Outline each blood parasite and name the species.
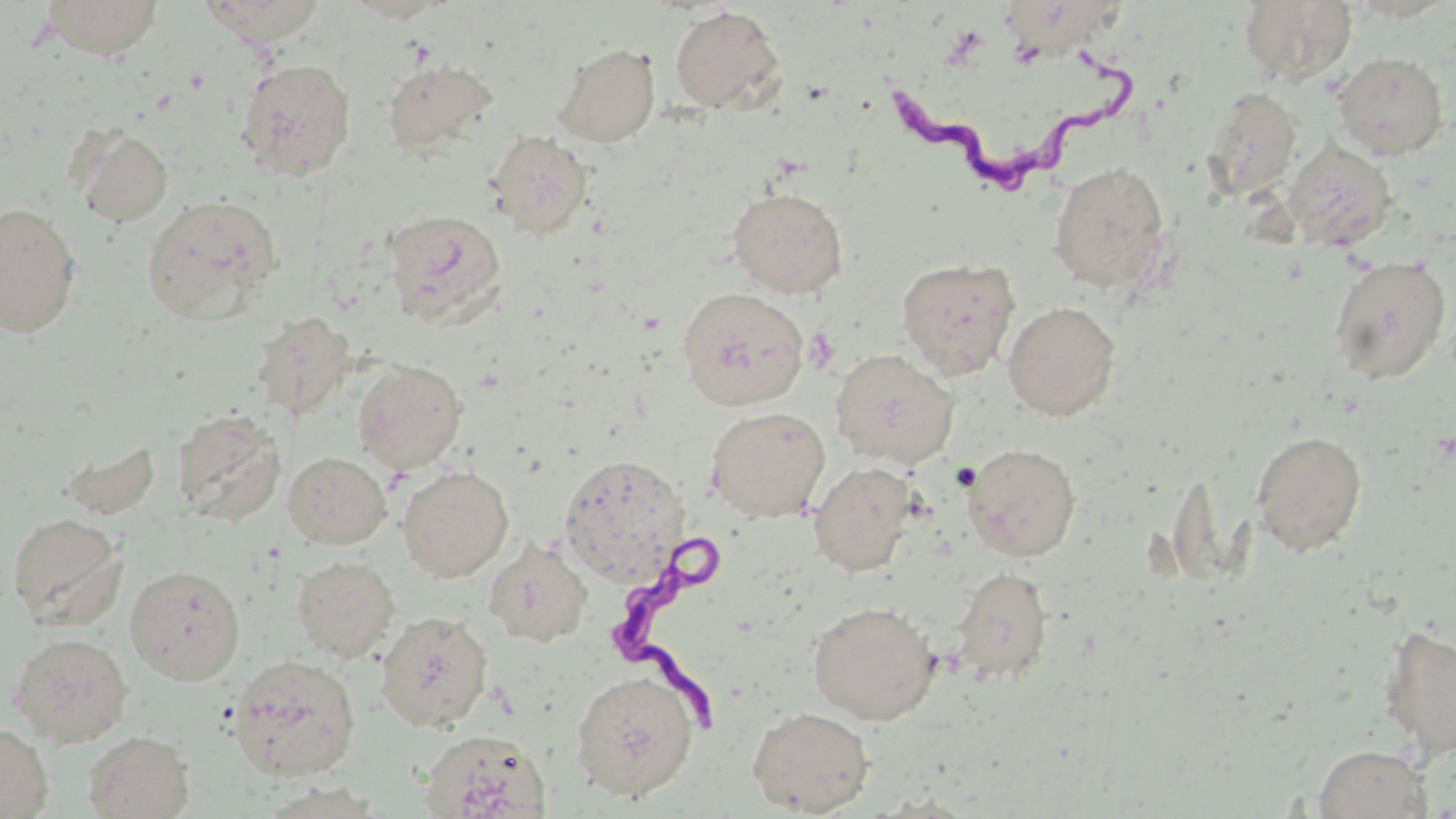
Approximate bounding boxes as named x1/y1/x2/y2 corners in pixels.
Trypanosoma brucei: (x1=871, y1=45, x2=1142, y2=194), (x1=599, y1=529, x2=727, y2=729).
No Plasmodium falciparum, Plasmodium ovale, Plasmodium malariae, Plasmodium vivax, or Babesia divergens observed.

Summary:
  - Platelet locations: (x1=803, y1=327, x2=840, y2=373)
  - Uninfected red blood cell locations: (x1=40, y1=0, x2=164, y2=59), (x1=201, y1=0, x2=330, y2=43), (x1=345, y1=0, x2=453, y2=22), (x1=1005, y1=0, x2=1129, y2=57), (x1=1238, y1=0, x2=1358, y2=85), (x1=669, y1=5, x2=786, y2=115), (x1=554, y1=42, x2=660, y2=147), (x1=1333, y1=52, x2=1449, y2=159), (x1=382, y1=58, x2=498, y2=159), (x1=236, y1=59, x2=356, y2=182), (x1=1201, y1=86, x2=1303, y2=202), (x1=71, y1=124, x2=173, y2=227), (x1=483, y1=129, x2=593, y2=240), (x1=1283, y1=139, x2=1397, y2=254), (x1=1048, y1=160, x2=1173, y2=293), (x1=727, y1=186, x2=849, y2=297), (x1=142, y1=195, x2=281, y2=322), (x1=0, y1=202, x2=82, y2=337), (x1=382, y1=210, x2=506, y2=324), (x1=1329, y1=255, x2=1452, y2=384), (x1=896, y1=257, x2=1020, y2=379), (x1=676, y1=287, x2=809, y2=410), (x1=1003, y1=300, x2=1121, y2=421), (x1=830, y1=349, x2=959, y2=469), (x1=352, y1=359, x2=467, y2=472), (x1=705, y1=406, x2=831, y2=522), (x1=170, y1=409, x2=287, y2=526), (x1=1251, y1=429, x2=1367, y2=556), (x1=963, y1=443, x2=1081, y2=561), (x1=284, y1=451, x2=392, y2=549), (x1=558, y1=455, x2=690, y2=583), (x1=808, y1=461, x2=919, y2=577), (x1=398, y1=466, x2=514, y2=582), (x1=6, y1=513, x2=125, y2=627), (x1=483, y1=538, x2=592, y2=647), (x1=292, y1=555, x2=399, y2=661), (x1=125, y1=563, x2=246, y2=684), (x1=951, y1=566, x2=1053, y2=683), (x1=807, y1=600, x2=941, y2=724), (x1=376, y1=610, x2=493, y2=731), (x1=1378, y1=622, x2=1455, y2=759), (x1=9, y1=632, x2=132, y2=746), (x1=228, y1=654, x2=361, y2=781), (x1=570, y1=670, x2=698, y2=801), (x1=746, y1=706, x2=875, y2=816), (x1=0, y1=722, x2=53, y2=818), (x1=420, y1=728, x2=552, y2=819), (x1=82, y1=729, x2=195, y2=818), (x1=1314, y1=744, x2=1432, y2=819)
  - Slide-level diagnosis: Trypanosoma brucei
  - Image size: 1456×819 pixels
  - Preparation: thin blood smear
  - Magnification: 1000x
  - Modality: light microscopy
  - Field of view: one of a larger specimen
  - Stain: May-Grünwald-Giemsa